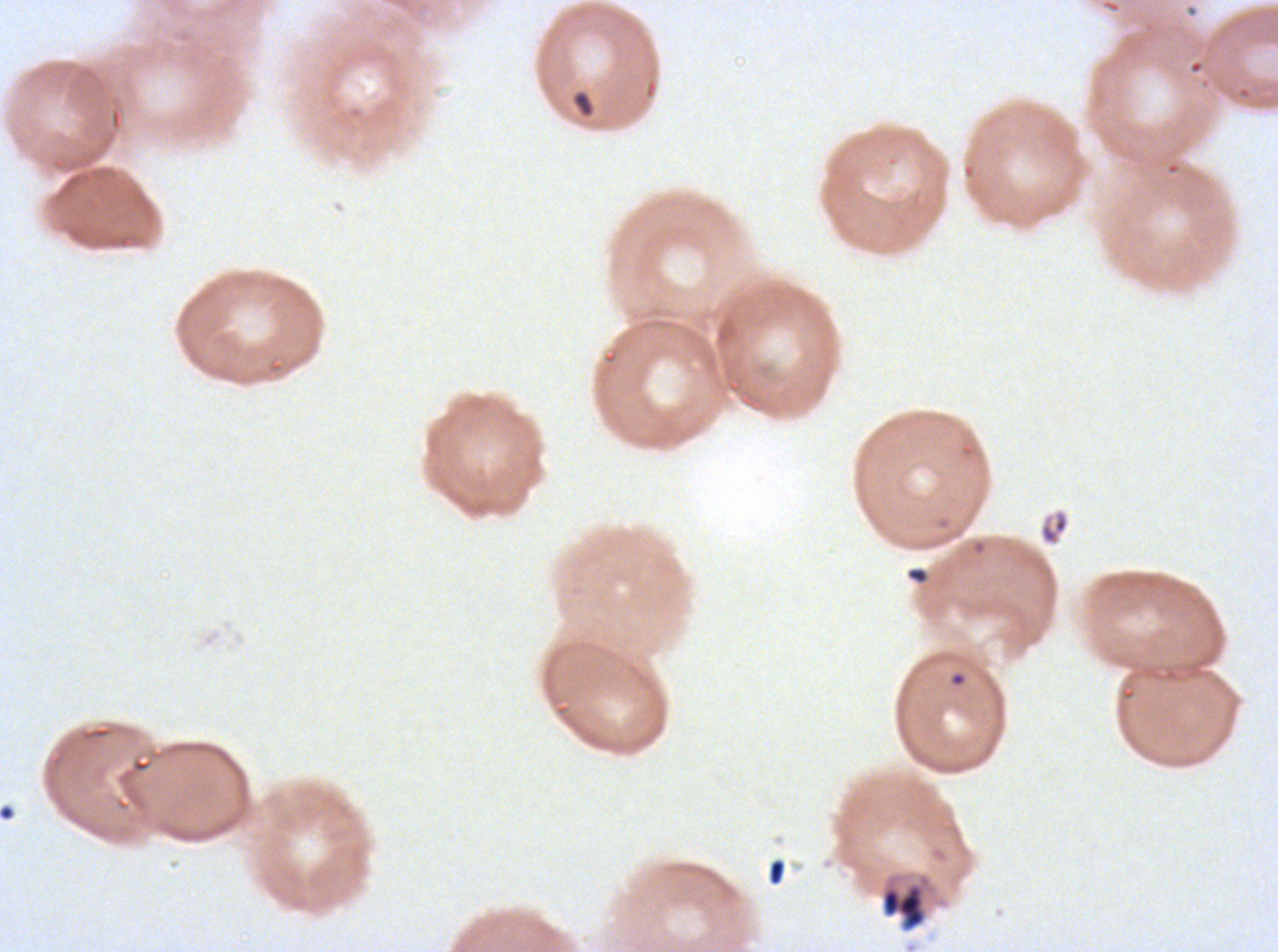

image_size: 1278×952 pixels
debris_locations: 'approximate bounding boxes as (x1, y1, x2, y2) in pixels: (571, 90, 596, 118), (1038, 508, 1070, 546), (905, 566, 930, 585), (767, 858, 787, 886), (879, 871, 939, 934)'
preparation: thin blood smear
field_of_view: sub-image separated from a larger composite
stain: Giemsa
specimen: ex-vivo P. falciparum culture from a patient in The Gambia, grown for 24 to 48 hours